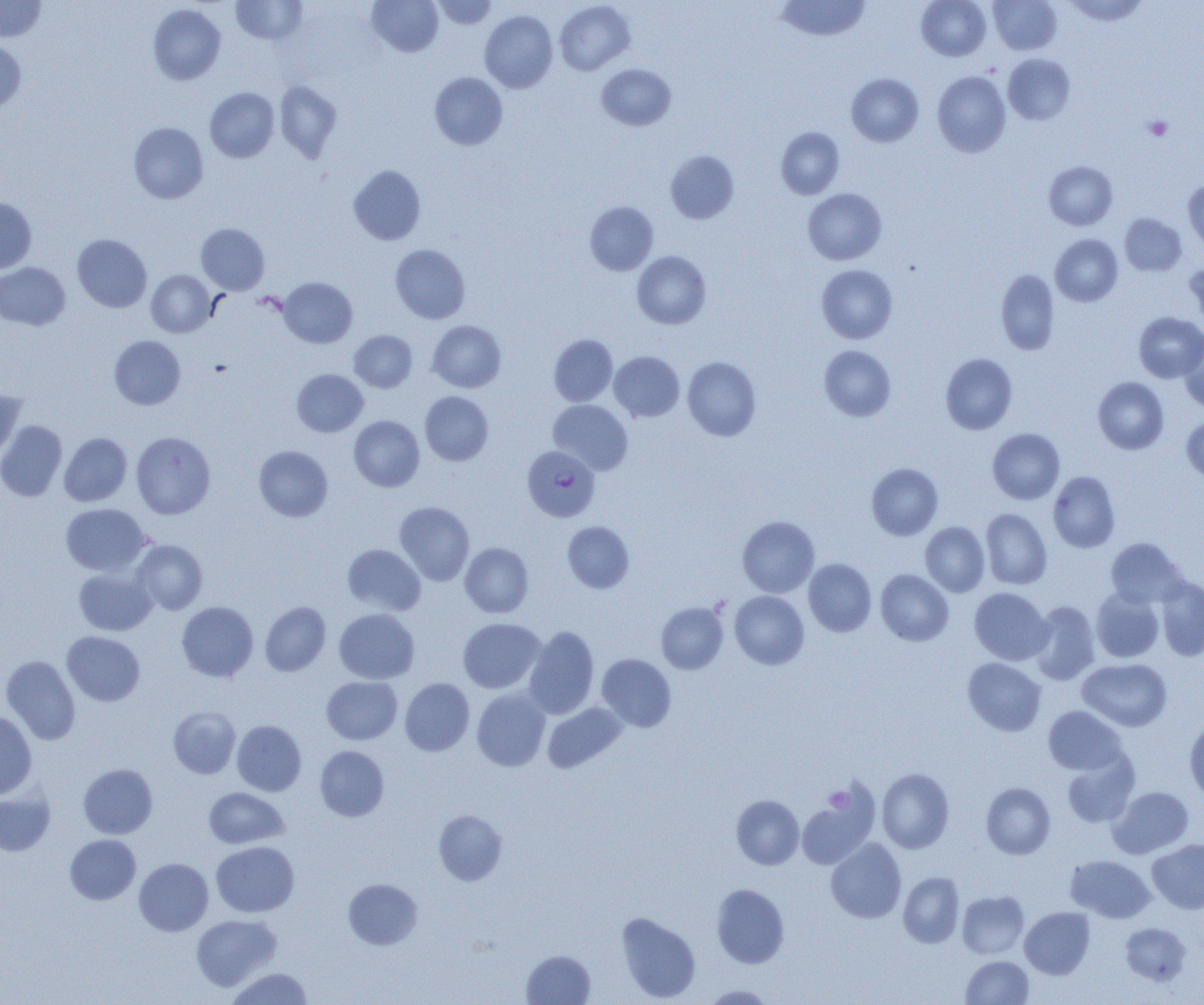 Approximate bounding boxes as (x1, y1, x2, y2) in pixels. Plasmodium falciparum-infected red blood cell locations: (522, 445, 599, 522). Platelet locations: (1144, 116, 1173, 141), (823, 787, 852, 813). Uninfected red blood cell locations: (231, 0, 308, 45), (367, 0, 443, 57), (432, 0, 498, 29), (776, 0, 870, 41), (916, 0, 991, 60), (988, 0, 1061, 54), (1063, 0, 1149, 25), (0, 1, 46, 42), (555, 1, 635, 75), (148, 4, 226, 85), (480, 10, 558, 93), (0, 40, 26, 114), (1003, 53, 1075, 125), (596, 63, 676, 130), (933, 71, 1011, 157), (430, 73, 507, 150), (846, 73, 924, 146), (274, 80, 342, 162), (205, 87, 279, 163), (128, 122, 208, 204), (776, 127, 844, 199), (665, 151, 739, 224), (1044, 161, 1117, 230), (349, 165, 425, 245), (1183, 180, 1204, 251), (803, 188, 886, 265), (0, 197, 36, 273), (585, 201, 658, 275), (1120, 214, 1186, 276), (196, 223, 270, 295), (72, 234, 152, 312), (1050, 234, 1122, 306), (390, 244, 470, 324), (632, 251, 711, 328), (1184, 260, 1204, 326), (0, 262, 70, 330), (816, 264, 898, 343), (996, 269, 1060, 355), (146, 270, 215, 337), (279, 277, 357, 348), (1134, 312, 1204, 382), (427, 320, 506, 393), (349, 330, 417, 392), (549, 334, 617, 406), (109, 335, 185, 409), (1178, 335, 1204, 412), (819, 345, 896, 421), (609, 351, 684, 422), (940, 353, 1017, 435), (682, 357, 761, 440), (292, 369, 368, 437), (1093, 377, 1168, 454), (0, 390, 26, 461), (420, 391, 493, 465), (549, 399, 633, 474), (349, 415, 424, 492), (1181, 417, 1204, 483), (0, 420, 67, 501), (988, 428, 1064, 504), (131, 431, 215, 519), (59, 432, 132, 506), (254, 445, 333, 521), (866, 463, 943, 540), (1048, 471, 1120, 552), (395, 502, 474, 585), (61, 503, 150, 576), (981, 508, 1052, 589), (737, 516, 819, 598), (562, 521, 634, 593), (921, 521, 989, 597), (1106, 538, 1187, 607), (131, 540, 207, 614), (460, 543, 533, 618), (343, 544, 425, 615), (803, 559, 876, 636), (74, 567, 157, 635), (876, 569, 953, 646), (1156, 577, 1204, 661), (969, 588, 1052, 665), (1091, 588, 1164, 662), (729, 591, 809, 669), (260, 601, 331, 676), (1029, 601, 1100, 685), (177, 602, 258, 681), (656, 602, 728, 674), (334, 608, 419, 683), (458, 618, 545, 693), (524, 627, 599, 719), (62, 631, 145, 706), (597, 654, 676, 732), (1, 655, 81, 745), (963, 658, 1046, 736), (1078, 658, 1172, 731), (322, 676, 402, 745), (400, 678, 474, 756), (472, 689, 550, 771), (543, 702, 627, 773), (168, 706, 240, 779), (1043, 706, 1127, 775), (0, 710, 37, 799), (1184, 718, 1204, 803), (232, 720, 306, 796), (315, 746, 389, 821), (1062, 751, 1140, 828), (79, 764, 157, 838), (877, 768, 954, 853), (981, 782, 1055, 859), (1108, 786, 1194, 858), (204, 787, 289, 849), (0, 789, 55, 856), (731, 795, 804, 870), (797, 796, 876, 868), (433, 809, 507, 886), (64, 834, 141, 904), (826, 838, 906, 923), (1147, 839, 1204, 914), (210, 841, 299, 917), (1066, 855, 1156, 923), (134, 858, 213, 936), (898, 872, 964, 948), (343, 878, 422, 950), (711, 884, 789, 968), (957, 891, 1029, 959), (1020, 907, 1095, 978), (616, 912, 700, 1002), (190, 914, 282, 990), (1120, 923, 1192, 986), (521, 950, 595, 1005), (961, 956, 1034, 1004), (225, 967, 314, 1005), (702, 985, 775, 1004). Slide-level diagnosis: Plasmodium falciparum. Image is 1204×1005 pixels. 1000x magnification. Light microscopy. One field of a larger specimen. Thin blood smear.